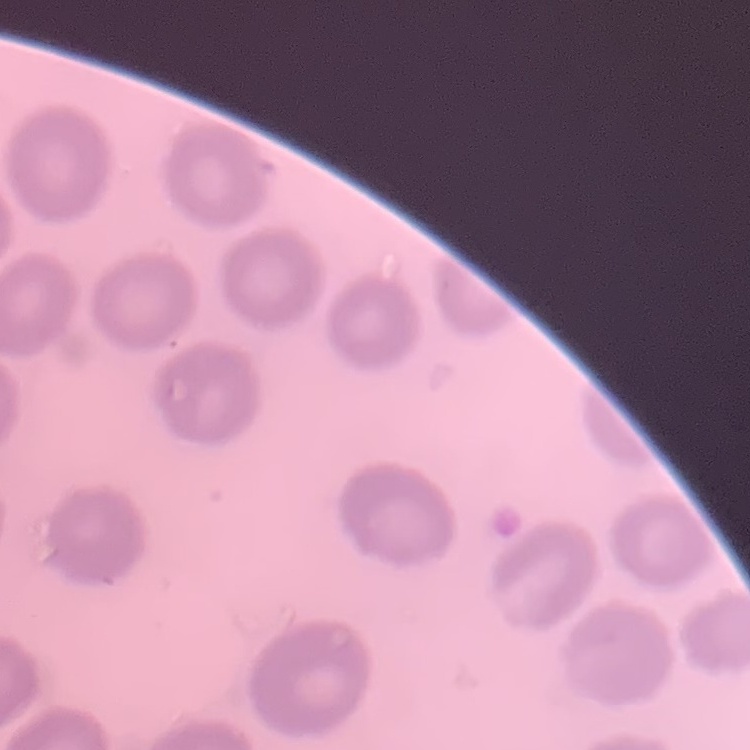
The erythrocytes exhibit no rouleaux formation. Thin peripheral smear. Field's or Giemsa stain. One tile cut from a larger photomicrograph.